Give the position of every malaria parasite.
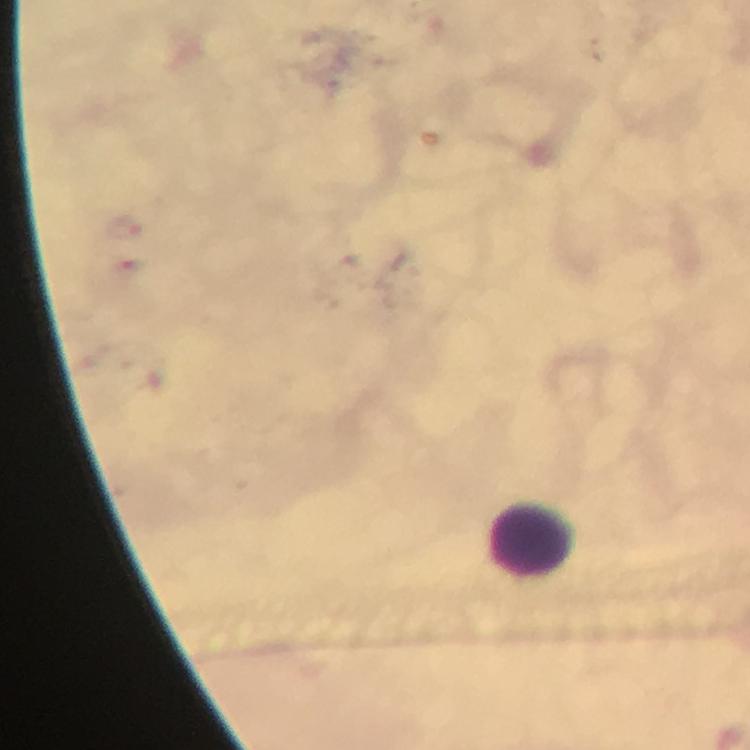
No malaria parasites detected.

Approximate centers as {x, y} in pixels.
Summary:
  - Leukocyte locations: {532, 542}
  - Capture: smartphone camera through the microscope
  - Context: from a malaria diagnostic workup
  - Immersion oil: applied
  - Stain: Giemsa
  - Preparation: thick smear
  - Image size: 750×750 pixels
  - Cropped from: a single field of view
  - Magnification: 100x